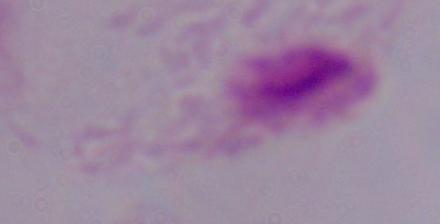

Summary:
  - Modality: micrograph
  - Identification: trichomonad
  - Magnification: 1000x